Classify this cell by malaria status.
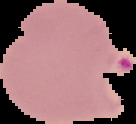
It is parasitized.

Segmented cell region on a black background. Image is 136×124 pixels. From a thin blood smear.